Give a bounding box for every Plasmodium parasite, every leukocyte, and every artifact (stain precipitate or debris).
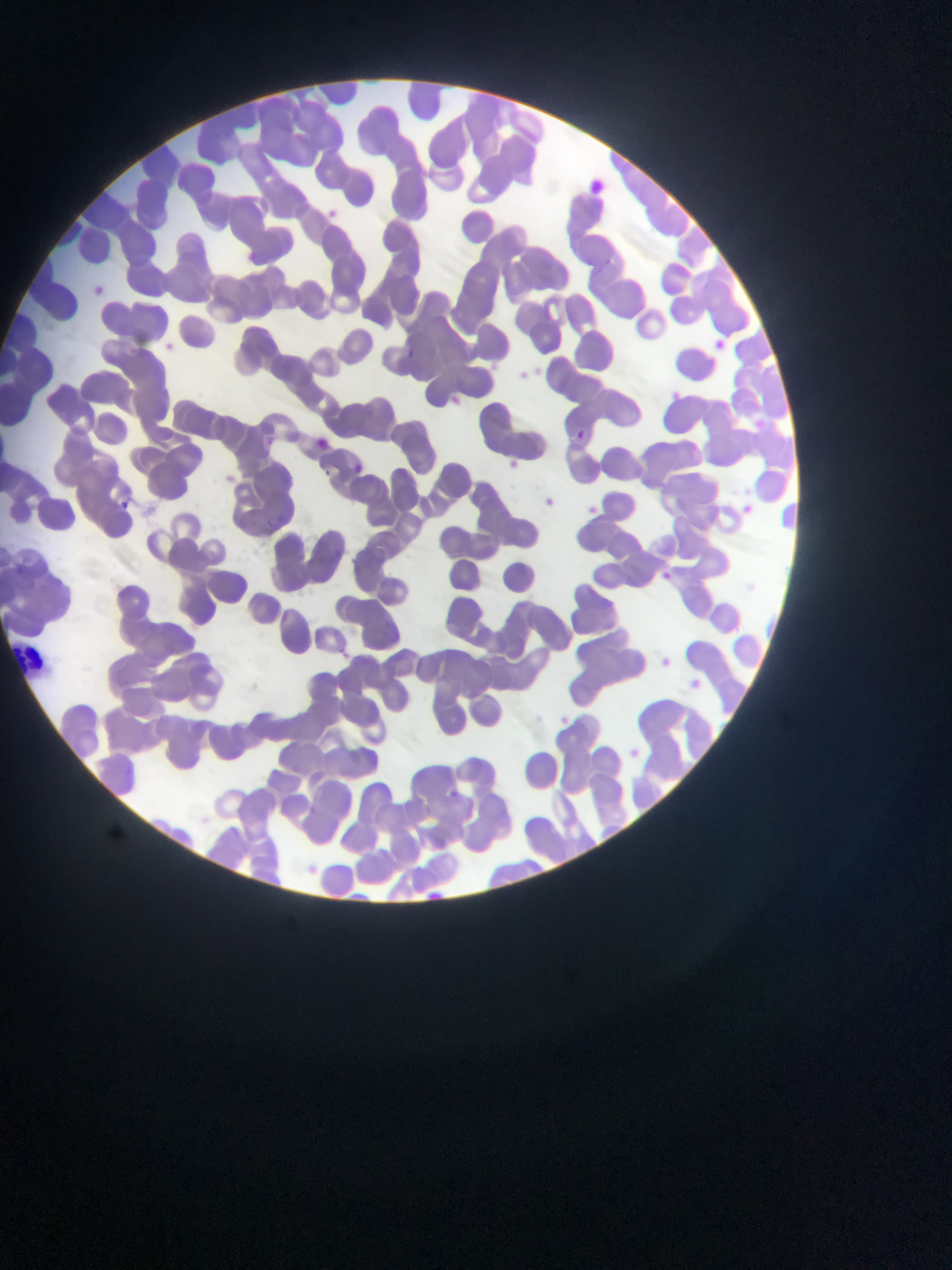

Approximate bounding boxes as [left, top, right, bottom] in pixels.
Plasmodium parasites: [84, 280, 112, 305], [709, 334, 732, 356], [405, 347, 423, 359], [670, 384, 690, 402], [745, 409, 770, 442], [568, 425, 591, 448], [307, 432, 337, 457], [345, 458, 370, 481], [536, 492, 560, 515], [121, 497, 136, 510], [582, 500, 603, 520], [738, 501, 758, 519], [658, 559, 679, 596], [9, 641, 44, 678], [656, 653, 676, 671], [684, 676, 705, 695], [623, 745, 644, 764].
No leukocytes observed.

Single field of view. Photographed through a microscope with a mobile-phone camera. Collected in Ghana. Thin blood film. Image is 952×1270 pixels.